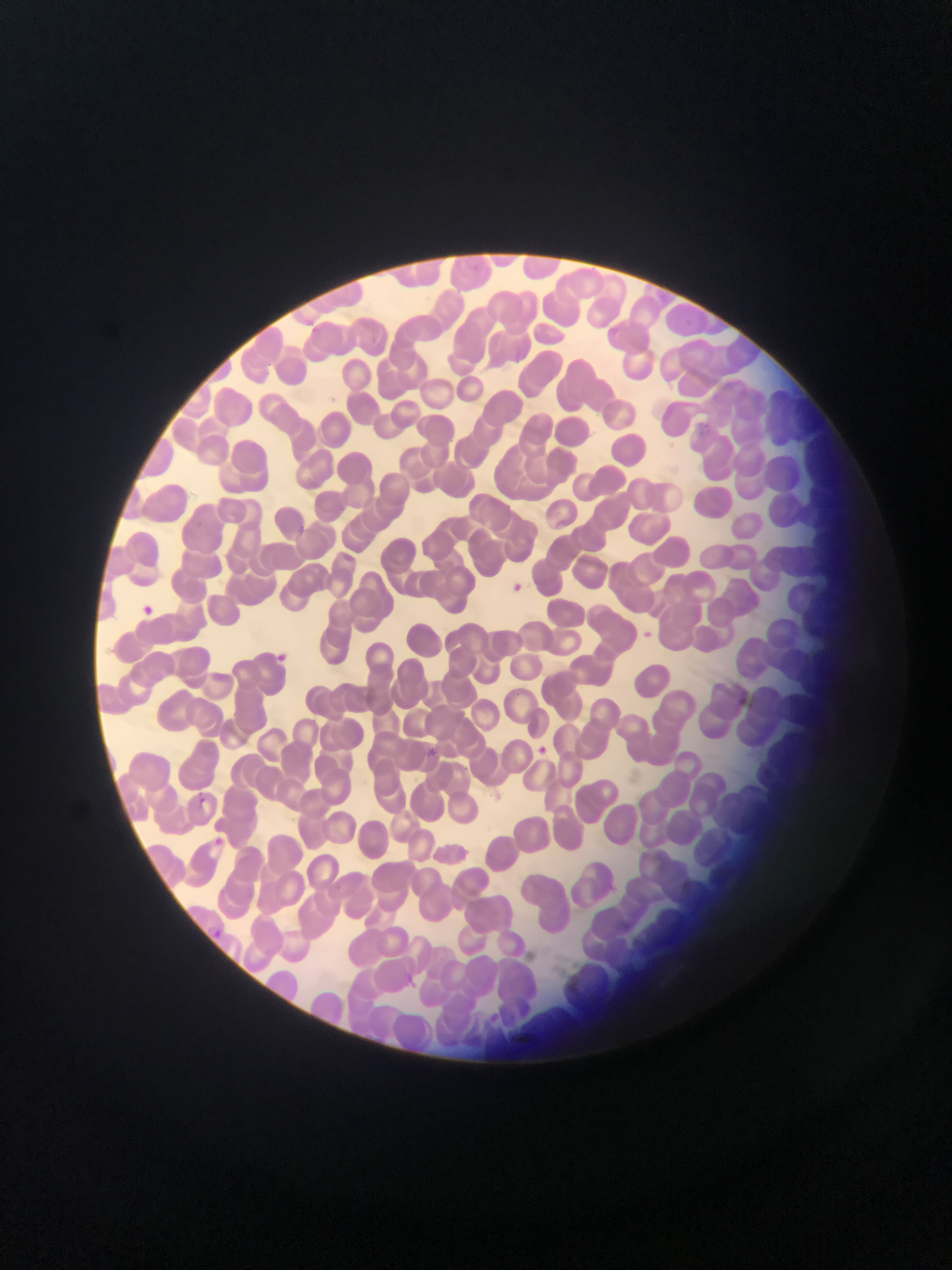

Approximate bounding boxes as (left, top, right, bottom) in pixels. Malaria parasite locations: (424, 741, 441, 760), (536, 741, 554, 760), (192, 789, 208, 799), (210, 835, 231, 843), (217, 926, 245, 946). Photographed through a microscope with a mobile-phone camera. Thin blood film. Collected in Ghana. Image is 952×1270 pixels. Single field of view.